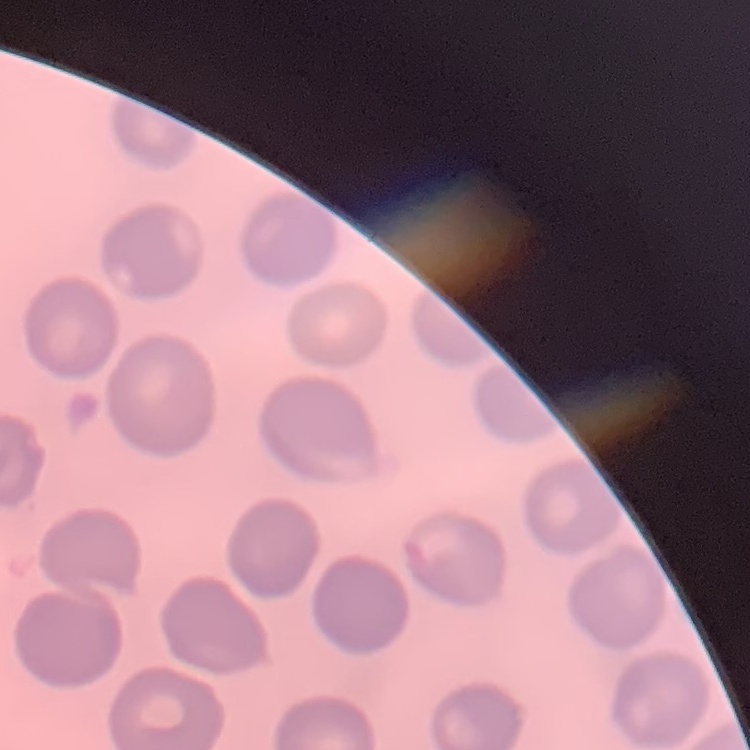

Summary:
  - Red blood cell morphology: no rouleaux formation
  - Stain: Field's or Giemsa
  - Image type: one tile cut from a larger photomicrograph
  - Preparation: thin blood film